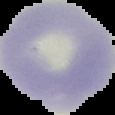

Summary:
  - Result: no Plasmodium parasites seen
  - Preparation: thin blood film
  - Image size: 115×115 pixels
  - Image type: segmented cell region on a black background